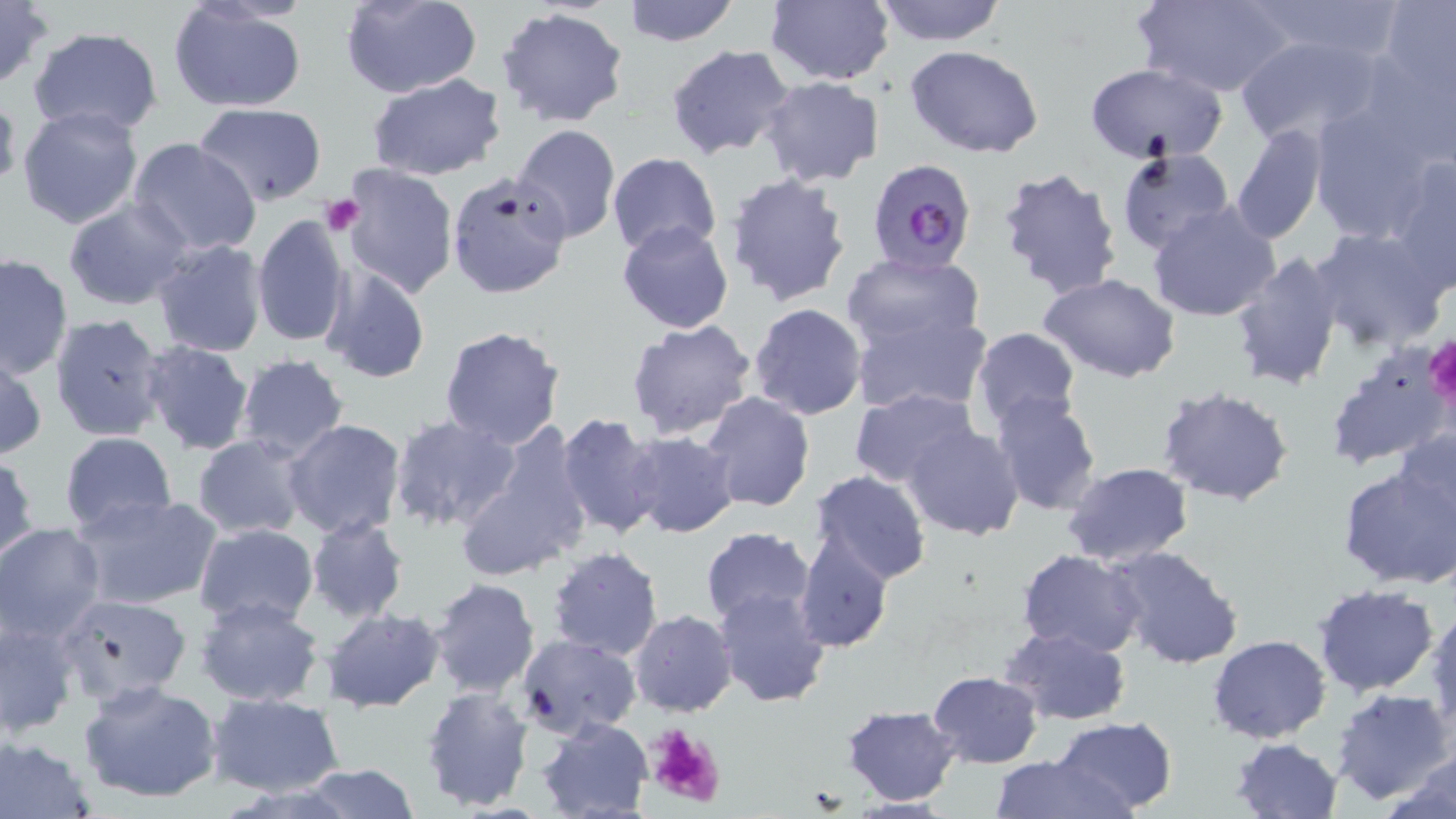

Approximate bounding boxes as (x1,y1)-(x2,y2) corner pairs in pixels. Plasmodium falciparum-infected red blood cell locations: (866,159)-(974,275). Platelet locations: (320,194)-(365,236), (1426,334)-(1456,416), (644,722)-(727,809). Uninfected red blood cell locations: (341,0)-(482,99), (621,0)-(741,46), (763,0)-(894,86), (871,0)-(1007,46), (1137,0)-(1293,98), (1246,0)-(1402,63), (0,1)-(52,89), (1376,1)-(1456,98), (168,3)-(308,114), (496,6)-(630,128), (27,27)-(164,137), (1235,32)-(1388,149), (665,44)-(794,159), (905,45)-(1045,160), (1356,48)-(1456,169), (1083,63)-(1228,164), (367,74)-(508,182), (761,77)-(886,187), (0,86)-(22,193), (193,103)-(328,204), (19,105)-(143,230), (1306,105)-(1441,242), (1231,122)-(1326,245), (510,124)-(622,245), (128,138)-(261,257), (1115,147)-(1235,258), (606,152)-(722,258), (1387,156)-(1456,295), (334,163)-(458,299), (994,165)-(1125,301), (724,172)-(855,309), (446,174)-(570,300), (64,198)-(193,311), (1147,202)-(1281,322), (252,212)-(350,351), (616,221)-(735,334), (1307,227)-(1449,351), (150,239)-(269,356), (1230,250)-(1346,391), (0,252)-(73,379), (842,252)-(984,352), (319,266)-(431,383), (1041,275)-(1181,383), (748,302)-(868,420), (848,309)-(991,417), (48,312)-(167,443), (625,318)-(758,441), (439,324)-(566,448), (969,325)-(1082,430), (139,341)-(254,456), (1322,343)-(1450,472), (1,352)-(47,461), (235,354)-(350,461), (1157,386)-(1296,507), (850,387)-(981,490), (701,392)-(815,512), (988,393)-(1102,517), (389,415)-(521,534), (556,416)-(660,537), (282,418)-(408,540), (902,424)-(1025,540), (1395,427)-(1455,538), (59,431)-(177,535), (624,431)-(741,539), (459,434)-(591,584), (193,435)-(309,538), (1,452)-(37,566), (1062,461)-(1193,567), (1337,462)-(1456,590), (806,471)-(931,587), (71,493)-(222,611), (305,516)-(409,623), (193,522)-(319,629), (0,523)-(106,643), (699,526)-(817,628), (795,532)-(893,655), (1106,543)-(1245,671), (546,546)-(665,661), (1017,550)-(1148,658), (428,577)-(541,698), (1312,584)-(1440,697), (714,587)-(833,709), (55,594)-(192,707), (195,596)-(326,707), (1427,600)-(1456,735), (320,607)-(446,712), (629,610)-(737,716), (0,615)-(80,739), (999,625)-(1131,727), (515,634)-(640,738), (1208,635)-(1331,743), (927,670)-(1044,767), (79,678)-(224,805), (420,684)-(535,812), (1330,687)-(1452,804), (208,693)-(344,797), (843,704)-(962,805), (1051,716)-(1178,815), (536,718)-(653,818), (0,736)-(97,817), (1230,736)-(1343,819), (989,752)-(1130,819), (1384,754)-(1456,819), (295,762)-(421,818). Slide-level diagnosis: Plasmodium falciparum. Light microscopy. Image is 1456×819 pixels. 1000x magnification. One field of a larger specimen. May-Grünwald-Giemsa stain. Thin blood smear.